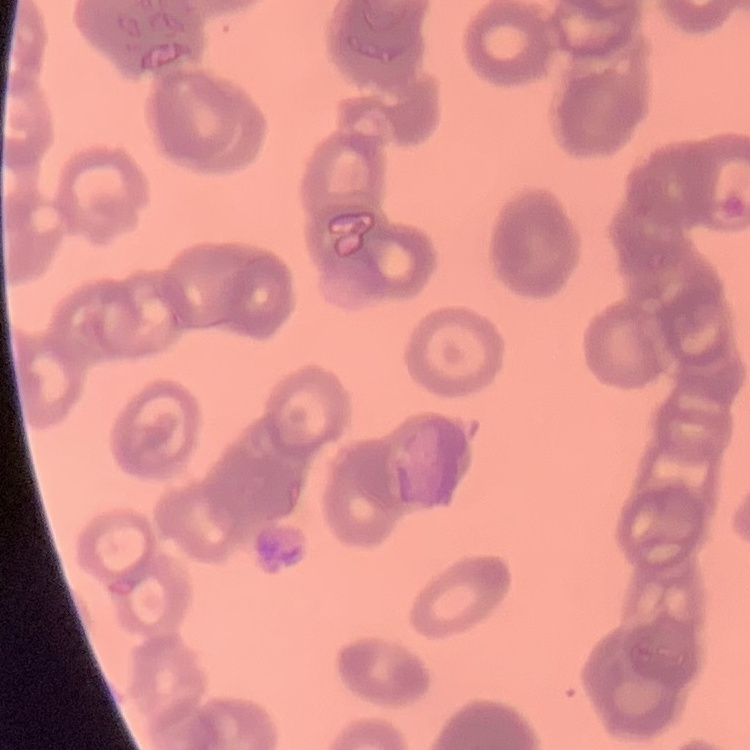

red blood cell morphology = rouleaux formation
image type = square crop of a larger photomicrograph
stain = Field's or Giemsa
preparation = thin blood film